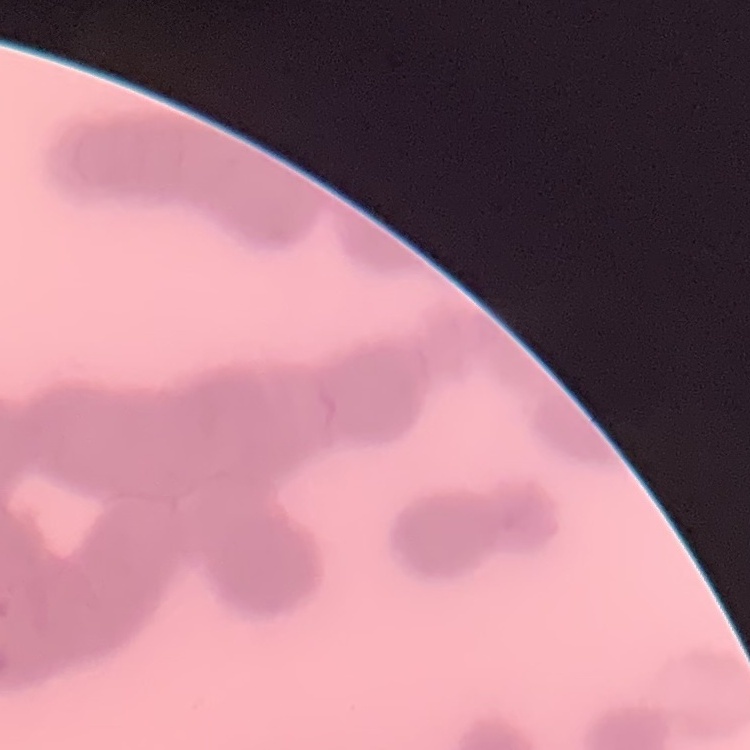
Summary:
  - Red blood cell morphology: rouleaux formation
  - Stain: Field's or Giemsa
  - Image type: one tile cut from a larger photomicrograph
  - Preparation: thin blood smear